Report the malaria status of this cell.
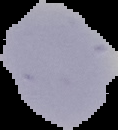
It is uninfected.

Summary:
  - Image type: cell region segmented out of the field of view; surrounding area masked to black
  - Preparation: thin blood smear
  - Image size: 118×130 pixels